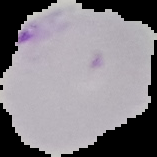
{
  "preparation": "thin blood film",
  "result": "malaria parasites detected",
  "image_type": "segmented cell region with the area outside set to black",
  "image_size": "157×157 pixels"
}